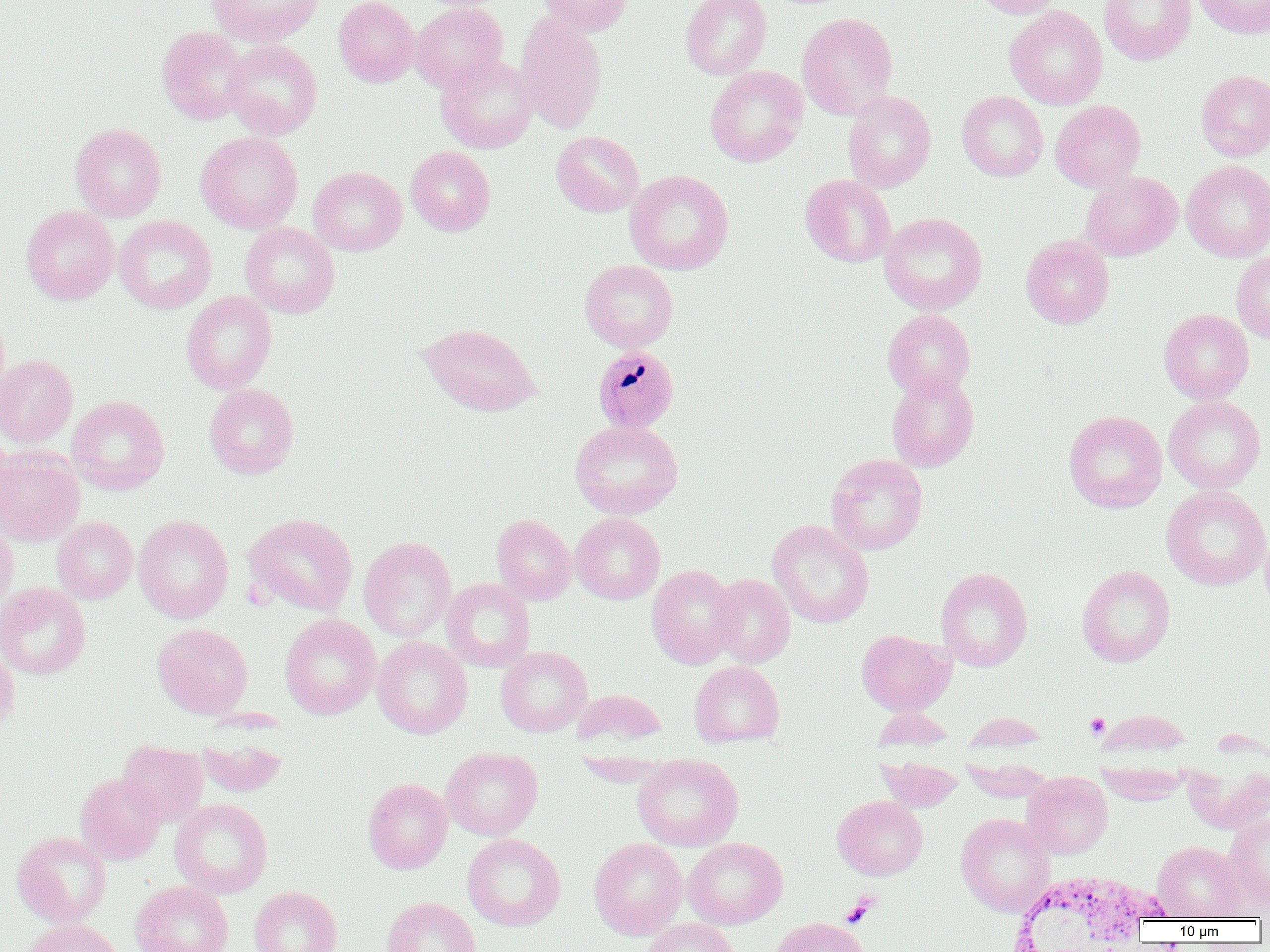

Summary:
  - Coordinate format: approximate bounding boxes as named x1/y1/x2/y2 corners in pixels
  - Uninfected red blood cell locations: (x1=206, y1=0, x2=323, y2=47), (x1=334, y1=0, x2=419, y2=88), (x1=413, y1=0, x2=508, y2=12), (x1=536, y1=0, x2=633, y2=37), (x1=680, y1=0, x2=771, y2=80), (x1=971, y1=0, x2=1065, y2=18), (x1=1099, y1=0, x2=1196, y2=65), (x1=1191, y1=0, x2=1270, y2=39), (x1=409, y1=2, x2=507, y2=93), (x1=1005, y1=3, x2=1196, y2=84), (x1=1005, y1=5, x2=1107, y2=109), (x1=515, y1=12, x2=608, y2=134), (x1=797, y1=12, x2=898, y2=120), (x1=157, y1=26, x2=250, y2=125), (x1=222, y1=39, x2=323, y2=139), (x1=436, y1=54, x2=538, y2=153), (x1=705, y1=65, x2=808, y2=167), (x1=1196, y1=69, x2=1270, y2=161), (x1=842, y1=90, x2=936, y2=193), (x1=957, y1=91, x2=1047, y2=181), (x1=1050, y1=100, x2=1146, y2=192), (x1=70, y1=123, x2=166, y2=221), (x1=196, y1=131, x2=303, y2=234), (x1=551, y1=131, x2=644, y2=217), (x1=405, y1=146, x2=495, y2=236), (x1=1181, y1=160, x2=1270, y2=261), (x1=308, y1=167, x2=406, y2=256), (x1=624, y1=170, x2=734, y2=275), (x1=1080, y1=171, x2=1182, y2=261), (x1=800, y1=174, x2=896, y2=268), (x1=21, y1=205, x2=119, y2=305), (x1=879, y1=212, x2=987, y2=315), (x1=114, y1=215, x2=217, y2=314), (x1=240, y1=222, x2=340, y2=318), (x1=1021, y1=235, x2=1114, y2=328), (x1=1232, y1=251, x2=1270, y2=343), (x1=579, y1=259, x2=678, y2=352), (x1=181, y1=291, x2=277, y2=394), (x1=882, y1=309, x2=976, y2=399), (x1=1158, y1=309, x2=1254, y2=403), (x1=418, y1=322, x2=542, y2=416), (x1=0, y1=355, x2=78, y2=448), (x1=886, y1=371, x2=979, y2=472), (x1=204, y1=383, x2=299, y2=479), (x1=67, y1=395, x2=169, y2=494), (x1=1163, y1=395, x2=1266, y2=493), (x1=1063, y1=410, x2=1167, y2=513), (x1=570, y1=419, x2=683, y2=519), (x1=0, y1=431, x2=17, y2=528), (x1=0, y1=447, x2=85, y2=546), (x1=826, y1=454, x2=928, y2=555), (x1=1161, y1=486, x2=1269, y2=591), (x1=570, y1=512, x2=665, y2=604), (x1=243, y1=513, x2=358, y2=616), (x1=133, y1=514, x2=233, y2=623), (x1=492, y1=514, x2=576, y2=605), (x1=52, y1=516, x2=137, y2=603), (x1=767, y1=519, x2=874, y2=628), (x1=0, y1=520, x2=18, y2=616), (x1=1260, y1=526, x2=1270, y2=620), (x1=358, y1=536, x2=457, y2=642), (x1=646, y1=564, x2=742, y2=668), (x1=1077, y1=564, x2=1175, y2=667), (x1=936, y1=567, x2=1033, y2=671), (x1=708, y1=573, x2=795, y2=668), (x1=442, y1=578, x2=535, y2=671), (x1=0, y1=583, x2=91, y2=680), (x1=279, y1=613, x2=380, y2=719), (x1=152, y1=622, x2=253, y2=719), (x1=856, y1=628, x2=954, y2=715), (x1=372, y1=637, x2=472, y2=739), (x1=0, y1=645, x2=20, y2=733), (x1=496, y1=646, x2=592, y2=736), (x1=689, y1=660, x2=785, y2=747), (x1=571, y1=688, x2=667, y2=751), (x1=198, y1=735, x2=286, y2=797), (x1=117, y1=741, x2=207, y2=827), (x1=441, y1=747, x2=543, y2=840), (x1=633, y1=753, x2=743, y2=851), (x1=877, y1=755, x2=963, y2=811), (x1=1022, y1=772, x2=1112, y2=858), (x1=75, y1=773, x2=165, y2=864), (x1=363, y1=777, x2=453, y2=874), (x1=832, y1=795, x2=928, y2=880), (x1=170, y1=798, x2=273, y2=898), (x1=1224, y1=810, x2=1270, y2=909), (x1=956, y1=813, x2=1055, y2=916), (x1=12, y1=831, x2=111, y2=927), (x1=462, y1=833, x2=566, y2=931), (x1=682, y1=837, x2=787, y2=928), (x1=588, y1=838, x2=687, y2=940), (x1=1152, y1=840, x2=1246, y2=921), (x1=130, y1=881, x2=234, y2=952), (x1=249, y1=886, x2=343, y2=952), (x1=382, y1=896, x2=481, y2=952), (x1=770, y1=917, x2=872, y2=952), (x1=20, y1=918, x2=123, y2=952), (x1=642, y1=918, x2=740, y2=952)
  - Plasmodium malariae-infected red blood cell locations: (x1=592, y1=345, x2=679, y2=433)
  - Platelet locations: (x1=1085, y1=713, x2=1110, y2=739), (x1=843, y1=897, x2=876, y2=926)
  - White blood cell locations: (x1=1003, y1=871, x2=1177, y2=951)
  - Slide-level diagnosis: Plasmodium malariae
  - Image size: 1270×952 pixels
  - Field of view: one of a larger specimen
  - Preparation: thin blood smear
  - Modality: optical microscopy
  - Magnification: 1000x